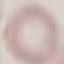

Summary:
  - Result: negative for malaria parasites
  - Capture: smartphone camera at the microscope eyepiece
  - Preparation: thin blood smear
  - Image type: automatically extracted cell patch, resized to 64 × 64 pixels
  - Stain: Giemsa